Assess this cell for malaria.
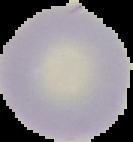
It is uninfected.

image_size: 133×142 pixels
preparation: thin blood film
image_type: segmented cell region on a black background